Point out each malaria parasite.
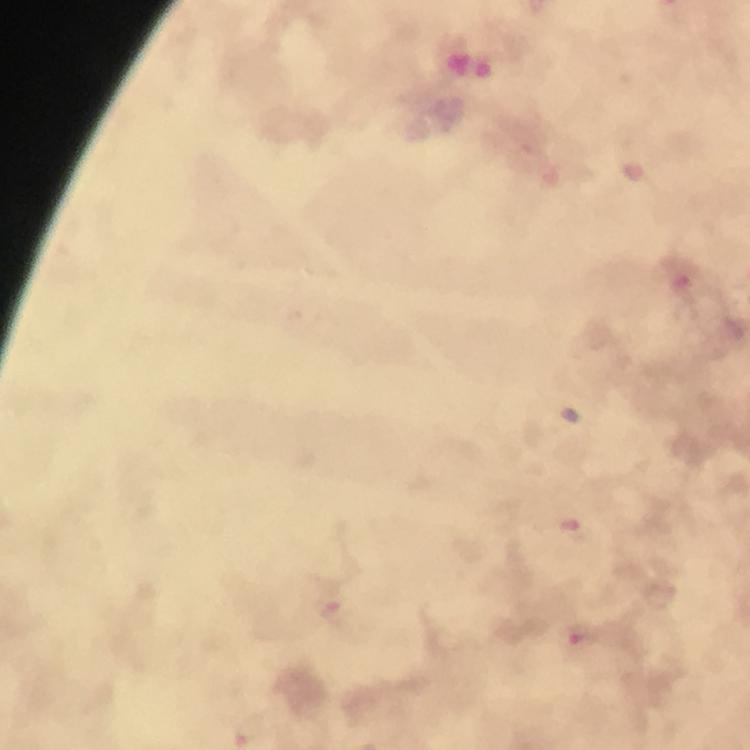

Approximate object centers, in pixels from the top-left corner.
Malaria parasites: (x=679, y=279), (x=570, y=526), (x=332, y=610), (x=581, y=636).

preparation = thick smear
capture = smartphone photograph through a microscope
context = from a malaria diagnostic workup
image size = 750×750 pixels
stain = Giemsa
magnification = 100x
immersion oil = used
cropped from = one field of view